Assess the morphology of the erythrocytes.
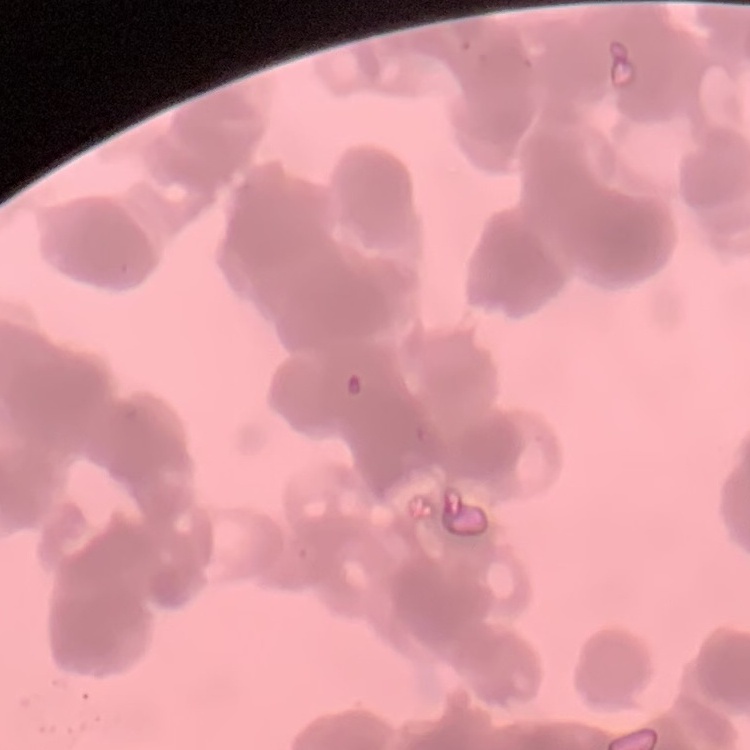

They show rouleaux formation.

Thin peripheral smear. Square crop of a larger photomicrograph. Stained with either Field's or Giemsa.